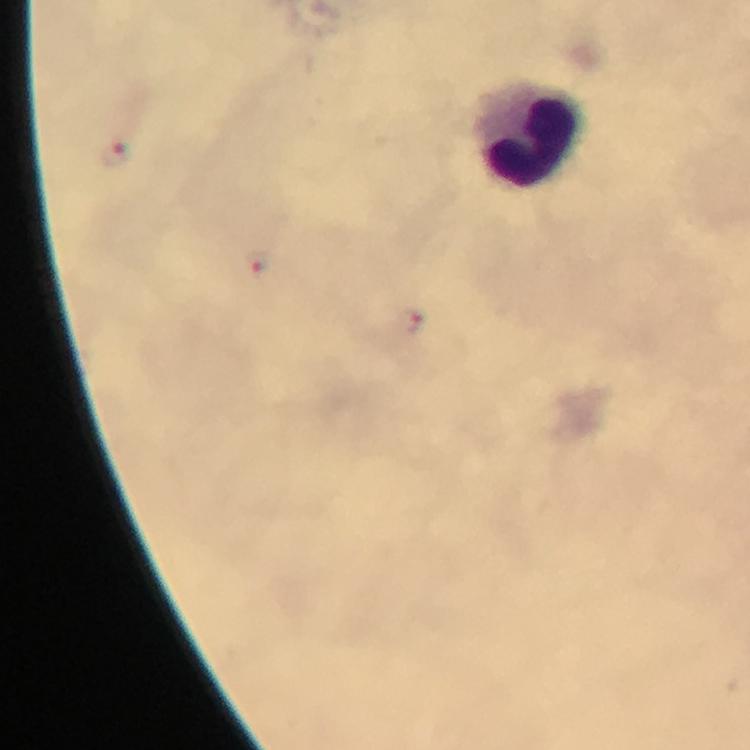

Approximate object centers, in pixels from the top-left corner. Malaria parasite locations: (x=114, y=154), (x=259, y=263), (x=409, y=322). Leukocyte locations: (x=532, y=133). Immersion oil was used. Cropped region of a single field of view. Thick blood film. 100x magnification. Giemsa-stained preparation. Image is 750×750 pixels. Photographed with a smartphone mounted on the microscope. From a malaria diagnostic workup.